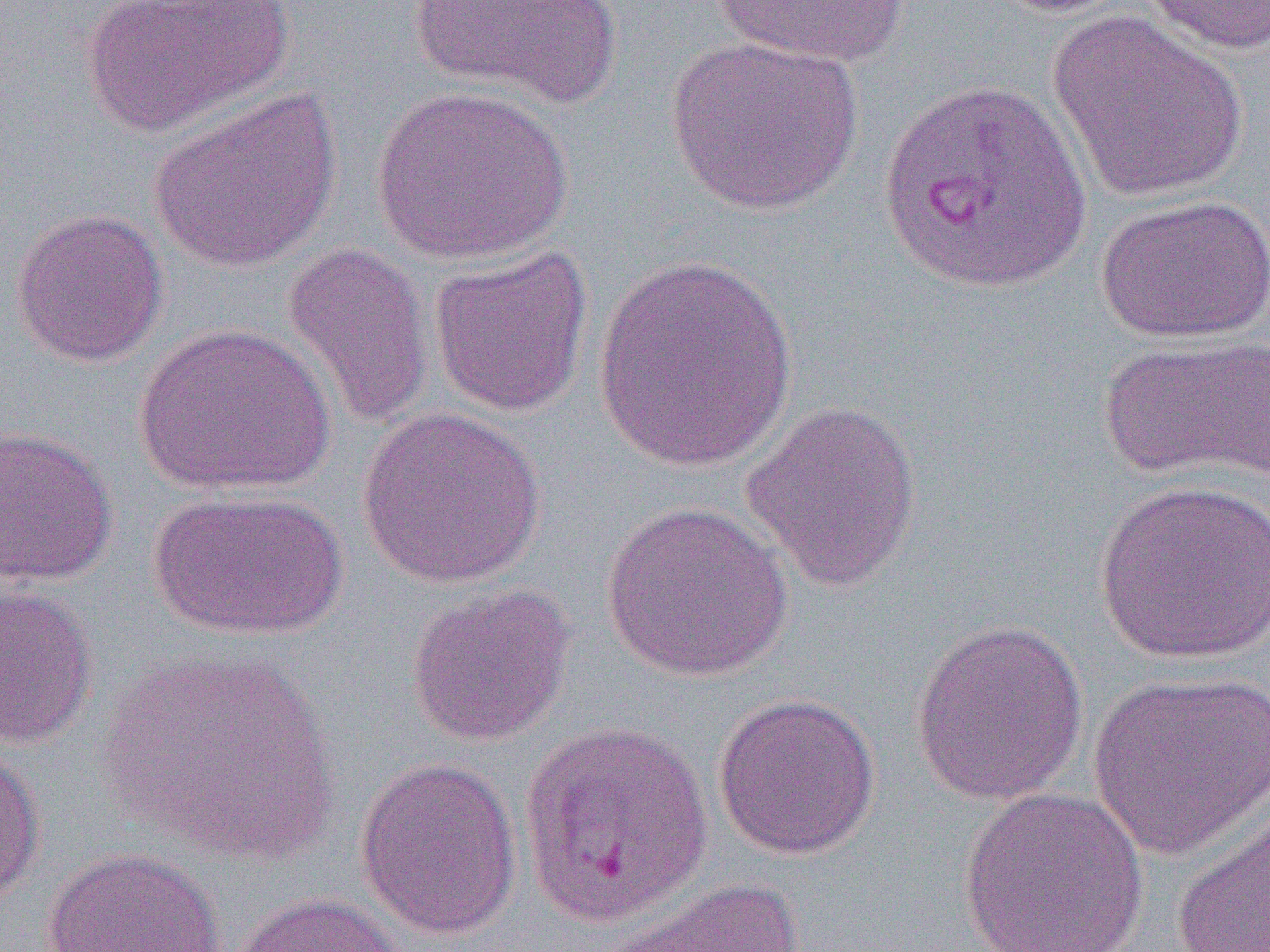

slide-level diagnosis = Plasmodium vivax
uninfected red blood cell locations = approximate bounding boxes as (x1, y1, x2, y2) in pixels: (80, 0, 293, 138), (409, 0, 623, 108), (711, 0, 909, 67), (983, 0, 1136, 18), (1137, 0, 1270, 54), (1046, 11, 1249, 202), (665, 37, 863, 216), (370, 86, 573, 264), (149, 88, 342, 273), (1095, 194, 1270, 343), (10, 209, 169, 368), (281, 241, 435, 431), (429, 244, 594, 419), (591, 256, 798, 471), (134, 323, 337, 497), (1098, 334, 1270, 484), (739, 399, 923, 593), (357, 407, 547, 589), (0, 425, 118, 587), (1093, 478, 1270, 665), (147, 490, 348, 640), (599, 501, 793, 682), (405, 583, 576, 747), (0, 585, 98, 749), (910, 619, 1089, 806), (97, 645, 339, 862), (1088, 669, 1270, 861), (711, 691, 882, 860), (518, 720, 713, 927), (0, 745, 46, 907), (355, 756, 523, 939), (958, 786, 1149, 952), (1170, 797, 1270, 952), (42, 847, 226, 952), (603, 877, 807, 952), (228, 891, 404, 952)
modality = optical microscopy
magnification = 1000x
Plasmodium vivax-infected red blood cell locations = approximate bounding boxes as (x1, y1, x2, y2) in pixels: (877, 76, 1092, 293)
preparation = thin blood smear
image size = 1270×952 pixels
field of view = one of a larger specimen